Give the preparation type.
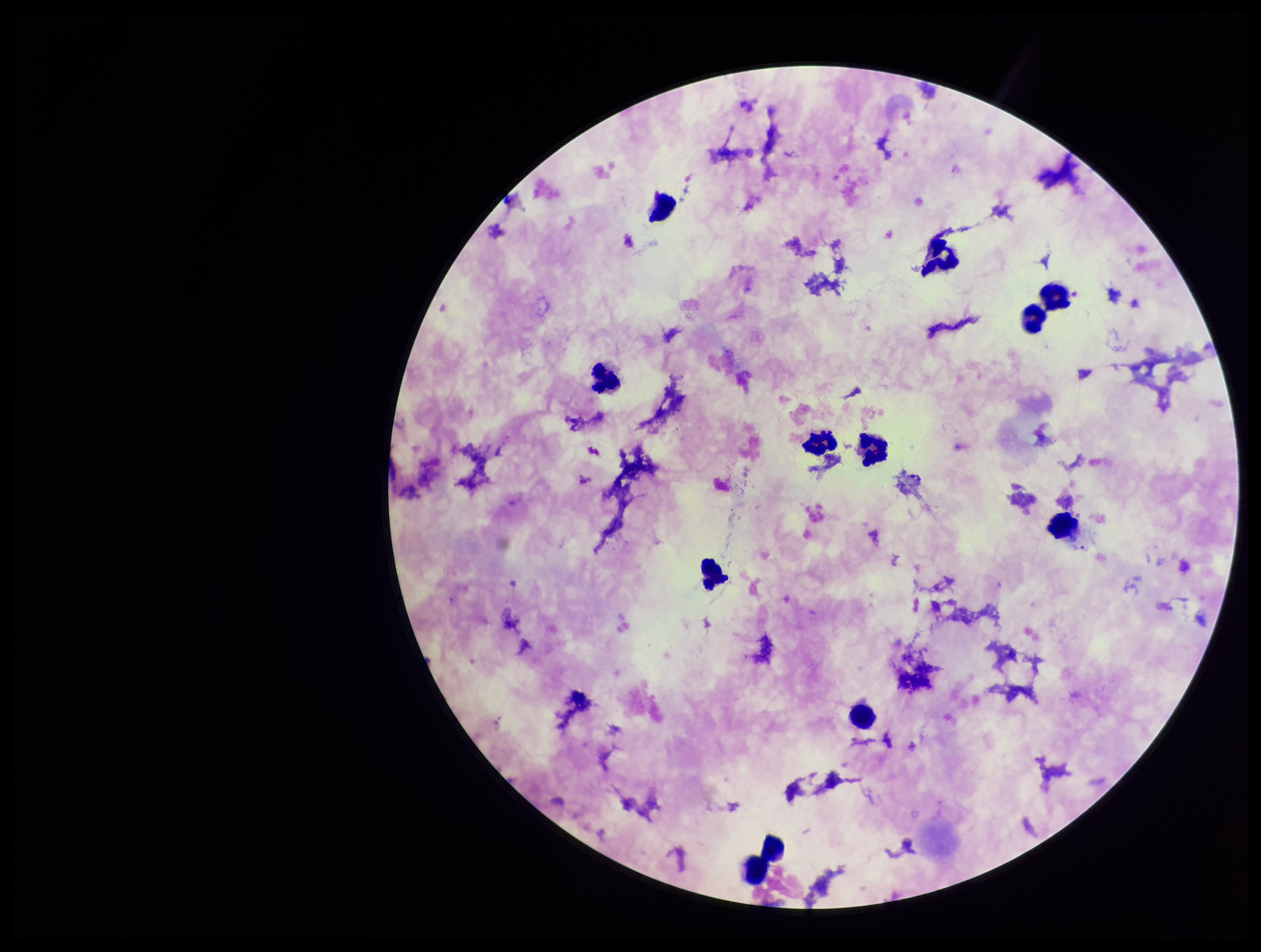
Thick.

parasite count = 0
capture = smartphone photograph through the microscope eyepiece
patient malaria status = positive
leukocyte count = 12
species reported for this patient = Plasmodium falciparum
stain = Giemsa
image size = 1261×952 pixels
Plasmodium parasites = none seen
field of view = single